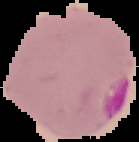

image size = 139×142 pixels
result = malaria parasites identified
image type = cell region segmented out of the field of view; surrounding area masked to black
preparation = thin blood smear